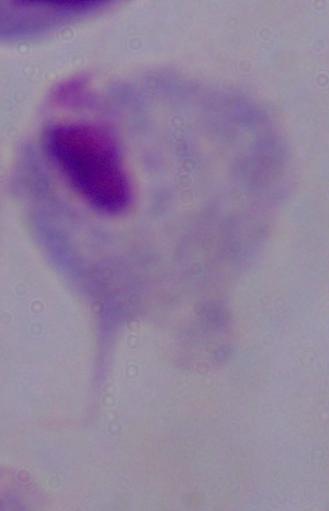
Summary:
  - Identification: trichomonad
  - Modality: photomicrograph
  - Magnification: 1000x